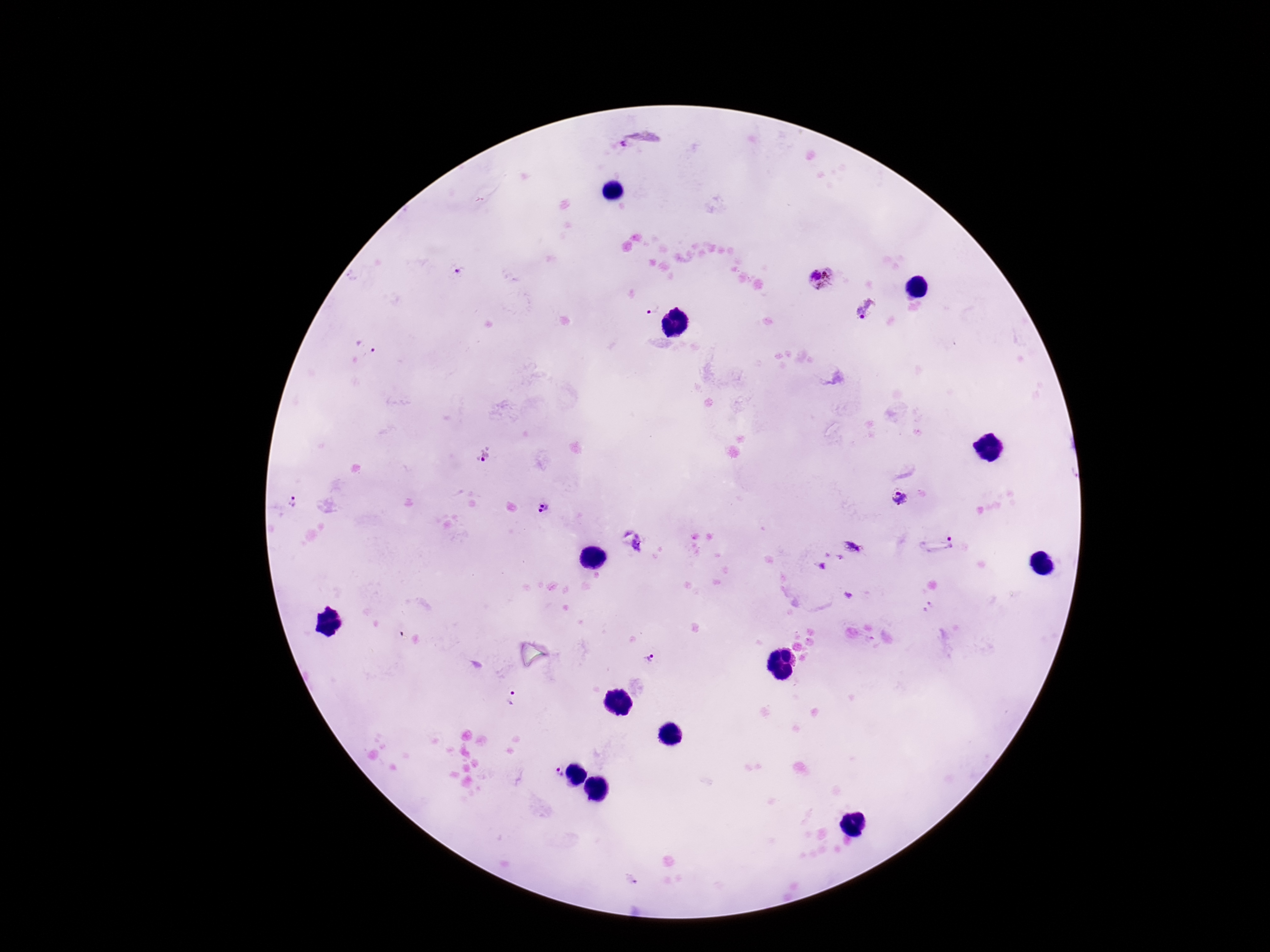

magnification = 100x
image size = 1270×952 pixels
patient malaria status = positive
field of view = single
Plasmodium parasite locations = approximate object centers, in pixels from the top-left corner: (x=640, y=141), (x=461, y=270), (x=823, y=280), (x=651, y=307), (x=868, y=309), (x=369, y=347), (x=483, y=456), (x=900, y=497), (x=292, y=502), (x=546, y=508), (x=632, y=539), (x=951, y=542), (x=853, y=547), (x=651, y=659), (x=512, y=699), (x=556, y=774)
preparation = thick blood film
stain = Giemsa
capture = smartphone camera through the microscope eyepiece